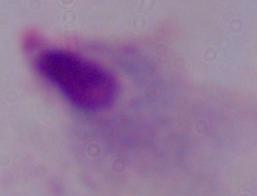

Summary:
  - Modality: photomicrograph
  - Identification: trichomonad
  - Magnification: 1000x